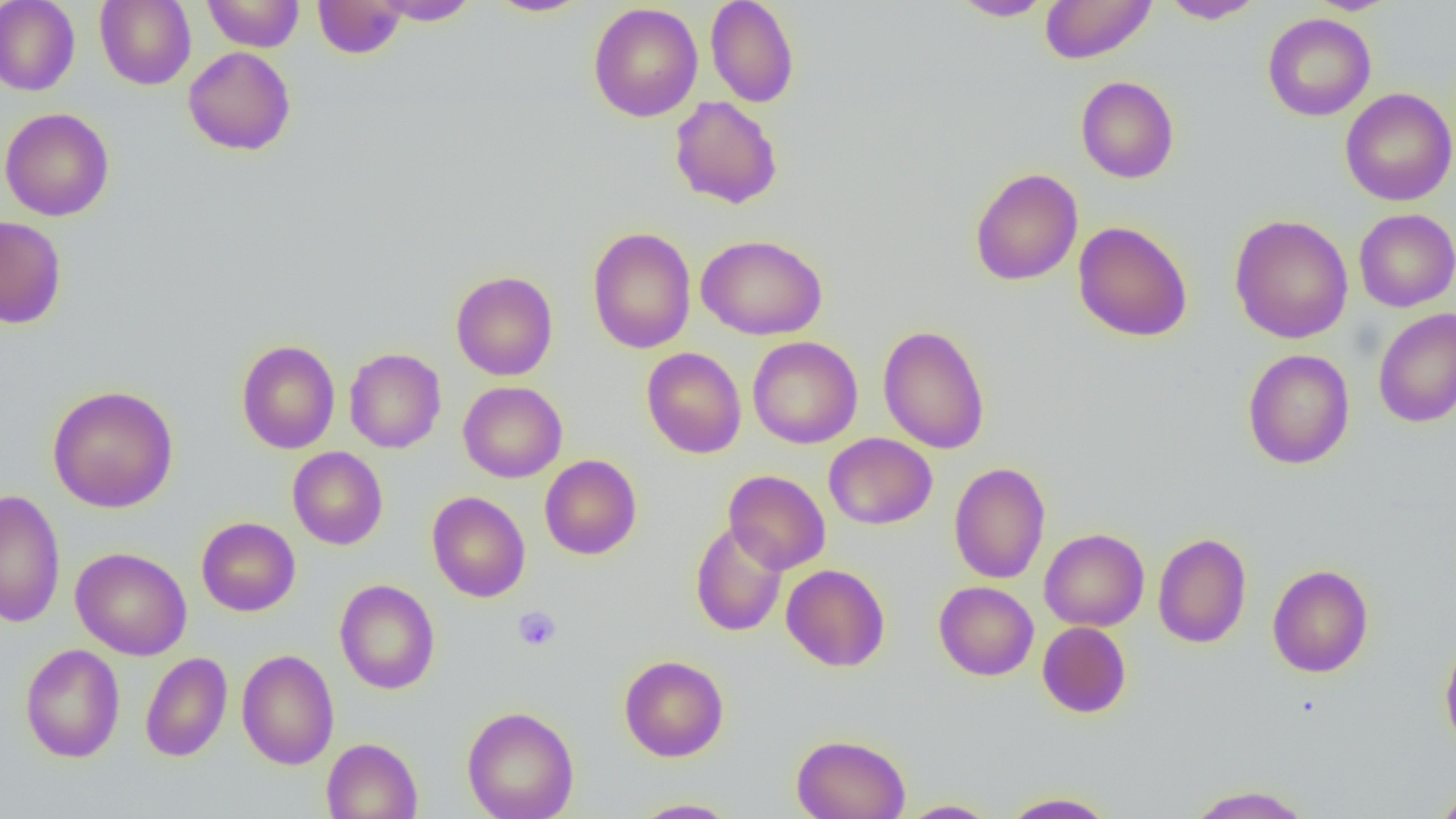
Summary:
  - Coordinate format: approximate bounding boxes as (x1,y1)-(x2,y2) corner pairs in pixels
  - Uninfected red blood cell locations: (0,0)-(80,96), (95,0)-(196,89), (202,0)-(305,52), (374,0)-(480,25), (485,0)-(593,17), (705,0)-(800,107), (950,0)-(1055,21), (1039,0)-(1156,64), (1160,0)-(1264,23), (1306,0)-(1400,15), (313,1)-(406,58), (588,3)-(703,122), (1262,13)-(1376,121), (183,46)-(296,156), (1076,76)-(1179,183), (1340,88)-(1456,206), (670,96)-(783,209), (0,107)-(115,221), (969,168)-(1083,286), (1354,209)-(1456,312), (1229,214)-(1353,343), (0,216)-(67,329), (1073,221)-(1193,342), (587,226)-(696,354), (696,234)-(827,340), (450,271)-(558,381), (1372,308)-(1456,427), (878,325)-(990,454), (747,336)-(862,448), (236,339)-(340,454), (641,347)-(746,459), (344,348)-(446,453), (1242,348)-(1355,469), (458,381)-(567,483), (47,385)-(179,513), (824,433)-(937,530), (287,447)-(388,549), (539,454)-(642,560), (949,462)-(1051,584), (723,470)-(831,574), (0,490)-(66,628), (427,491)-(530,602), (196,517)-(301,616), (690,521)-(788,637), (1039,528)-(1149,631), (1152,532)-(1252,648), (70,546)-(192,661), (781,564)-(890,672), (1267,564)-(1374,678), (335,579)-(440,694), (934,581)-(1039,681), (1037,622)-(1131,718), (1439,637)-(1456,756), (20,643)-(125,763), (237,649)-(339,770), (140,652)-(232,762), (619,655)-(729,761), (462,706)-(579,819), (791,734)-(910,819), (322,737)-(422,819), (1183,784)-(1316,819), (1431,787)-(1456,818), (1000,791)-(1120,818), (630,798)-(741,818), (897,799)-(1002,818)
  - Platelet locations: (513,605)-(562,651)
  - Slide-level diagnosis: no evidence of blood parasites
  - Magnification: 1000x
  - Modality: optical microscopy
  - Preparation: thin blood smear
  - Image size: 1456×819 pixels
  - Field of view: single